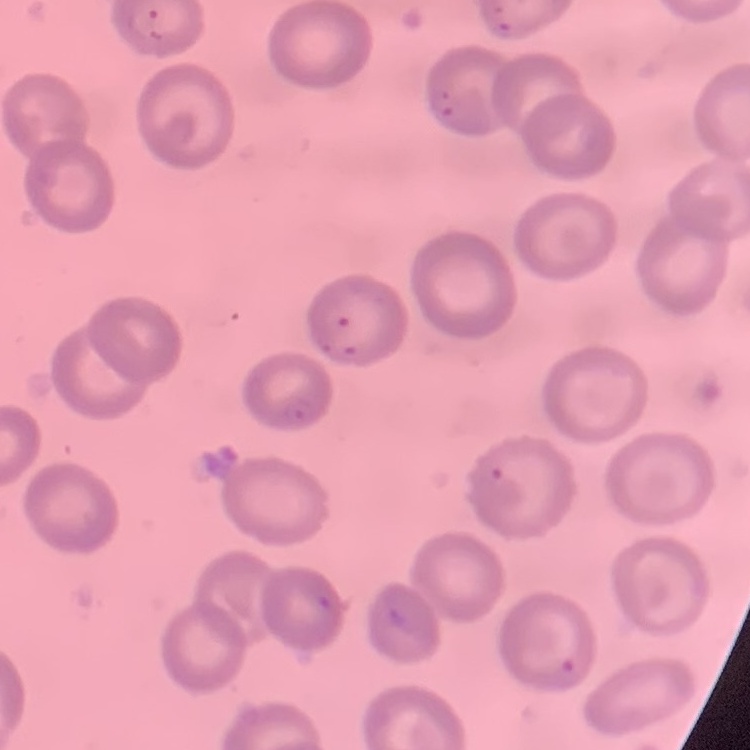

Summary:
  - Erythrocyte morphology: no rouleaux formation
  - Preparation: thin blood smear
  - Stain: Field's or Giemsa
  - Image type: square crop of a larger photomicrograph